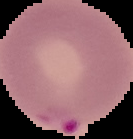
image size = 133×139 pixels
preparation = thin blood smear
malaria status = parasitized
image type = segmented cell region on a black background